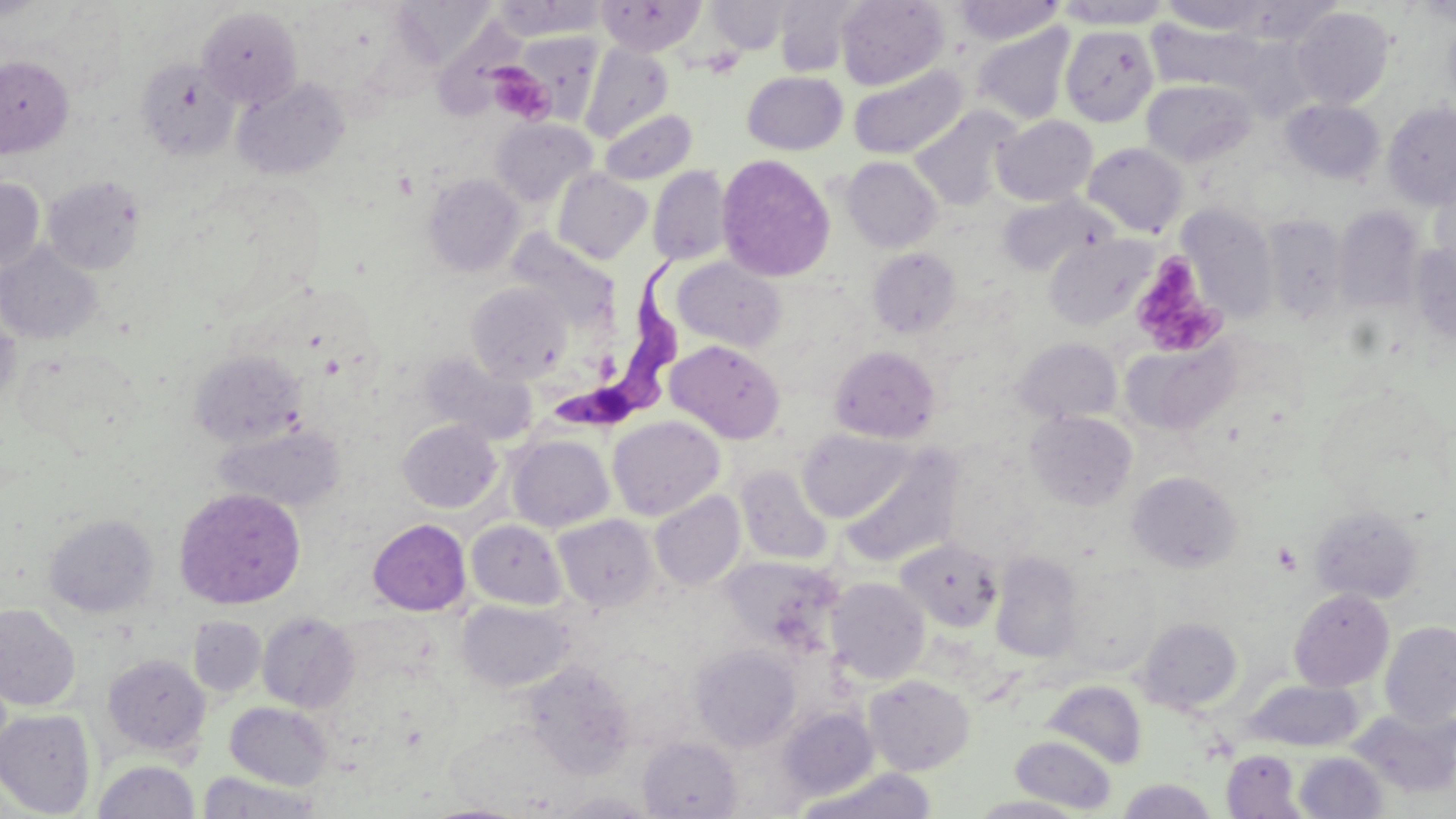
Summary:
  - Coordinate format: approximate bounding boxes as [x1, y1, x2, y2] in pixels
  - Trypanosoma brucei locations: [550, 255, 685, 440]
  - Platelet locations: [485, 62, 555, 124], [1129, 252, 1225, 358]
  - Uninfected red blood cell locations: [0, 0, 49, 20], [491, 0, 606, 40], [597, 0, 706, 55], [706, 0, 793, 54], [773, 0, 868, 76], [835, 0, 949, 90], [1235, 0, 1341, 43], [1412, 0, 1456, 25], [953, 1, 1063, 44], [1054, 1, 1172, 28], [1157, 1, 1272, 34], [197, 6, 303, 109], [1291, 7, 1395, 109], [433, 17, 528, 119], [971, 23, 1076, 125], [1060, 24, 1159, 126], [509, 32, 603, 125], [580, 43, 674, 143], [0, 56, 73, 157], [136, 58, 240, 160], [848, 65, 969, 160], [742, 71, 848, 155], [232, 77, 350, 180], [1141, 78, 1256, 168], [1281, 99, 1385, 183], [1383, 102, 1456, 209], [911, 107, 1021, 210], [600, 109, 696, 185], [992, 115, 1097, 206], [491, 119, 597, 207], [1083, 143, 1188, 237], [716, 154, 836, 283], [841, 156, 942, 253], [648, 166, 732, 266], [552, 168, 653, 264], [1429, 173, 1456, 278], [423, 174, 524, 277], [42, 175, 145, 274], [0, 177, 44, 273], [997, 193, 1114, 277], [1177, 203, 1278, 324], [1335, 207, 1424, 312], [1262, 215, 1350, 326], [510, 230, 616, 327], [1044, 234, 1155, 331], [0, 243, 102, 344], [1409, 243, 1456, 346], [868, 247, 962, 338], [673, 257, 786, 352], [467, 282, 572, 383], [1, 308, 20, 412], [1013, 337, 1122, 424], [1122, 338, 1240, 436], [666, 340, 785, 443], [829, 345, 941, 443], [17, 347, 141, 455], [190, 350, 306, 447], [421, 354, 537, 446], [1026, 410, 1138, 511], [608, 416, 725, 520], [398, 420, 502, 512], [215, 423, 344, 512], [797, 428, 916, 523], [507, 435, 614, 532], [841, 448, 964, 569], [736, 465, 833, 565], [1127, 471, 1242, 572], [173, 487, 306, 609], [650, 491, 746, 590], [1309, 505, 1424, 604], [44, 514, 159, 617], [553, 514, 658, 612], [368, 519, 471, 615], [466, 519, 568, 609], [896, 537, 1004, 633], [990, 552, 1083, 663], [720, 556, 843, 654], [1062, 562, 1161, 675], [826, 577, 930, 685], [1289, 588, 1394, 692], [458, 600, 574, 692], [0, 604, 80, 710], [258, 613, 359, 713], [188, 616, 266, 697], [1137, 617, 1242, 714], [1380, 620, 1456, 729], [691, 644, 802, 750], [102, 654, 211, 758], [522, 661, 637, 777], [864, 675, 975, 775], [1244, 679, 1363, 751], [1043, 680, 1147, 769], [225, 702, 333, 791], [779, 707, 879, 801], [1349, 707, 1456, 800], [0, 708, 96, 818], [1010, 735, 1117, 814], [638, 736, 742, 818], [1220, 750, 1306, 817], [1294, 751, 1388, 818], [93, 760, 200, 818], [795, 768, 938, 819], [198, 770, 322, 817], [1117, 779, 1218, 818], [968, 795, 1091, 818], [419, 803, 530, 819]
  - Slide-level diagnosis: Trypanosoma brucei
  - Image size: 1456×819 pixels
  - Stain: May-Grünwald-Giemsa
  - Preparation: thin blood smear
  - Modality: light microscopy
  - Field of view: one of a larger specimen
  - Magnification: 1000x